Locate Plasmodium parasites and leukocytes.
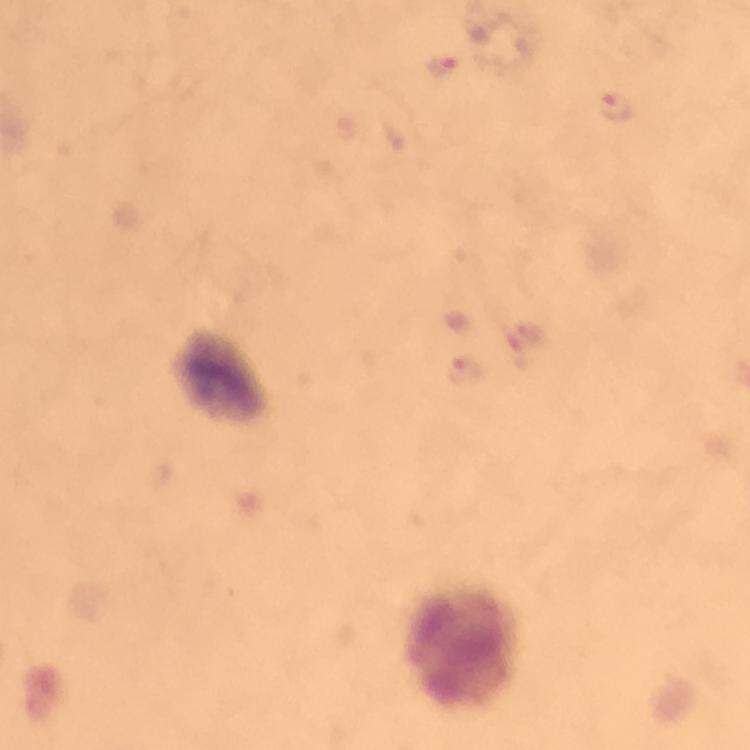

Approximate centers as {x, y} in pixels.
Plasmodium parasites: {441, 68}, {616, 107}.
Leukocytes: {224, 377}, {463, 648}.

Summary:
  - Magnification: 100x
  - Preparation: thick blood smear
  - Cropped from: a single field of view
  - Image size: 750×750 pixels
  - Immersion oil: applied
  - Capture: smartphone mounted on the microscope
  - Stain: Giemsa
  - Context: from a diagnostic examination for malaria